Locate every malaria parasite.
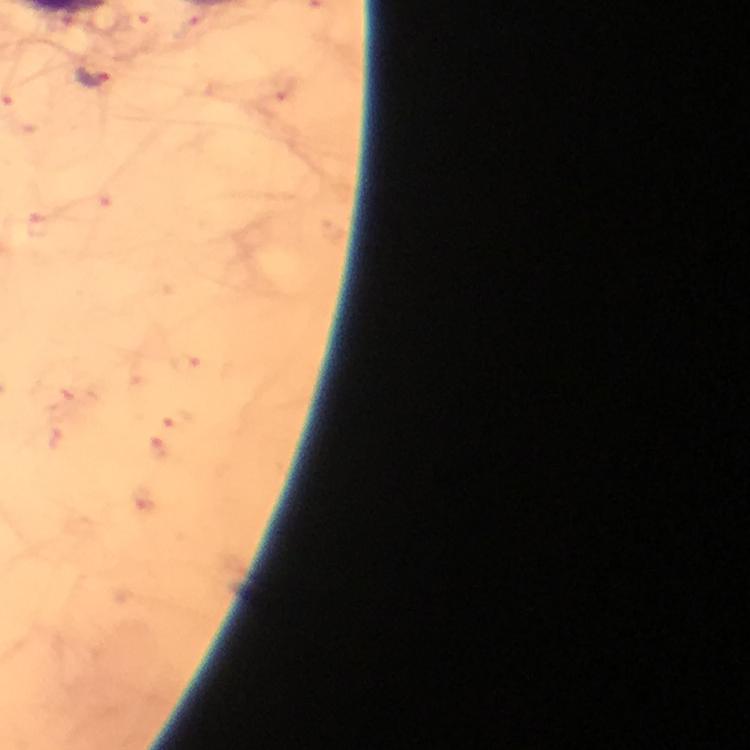

Approximate object centers, in pixels from the top-left corner.
Malaria parasites: (x=94, y=77).

stain = Giemsa
context = from a malaria diagnostic workup
image size = 750×750 pixels
immersion oil = applied
preparation = thick smear
magnification = 100x
cropped from = a single field of view
capture = smartphone camera through the microscope